Locate and identify every blood parasite.
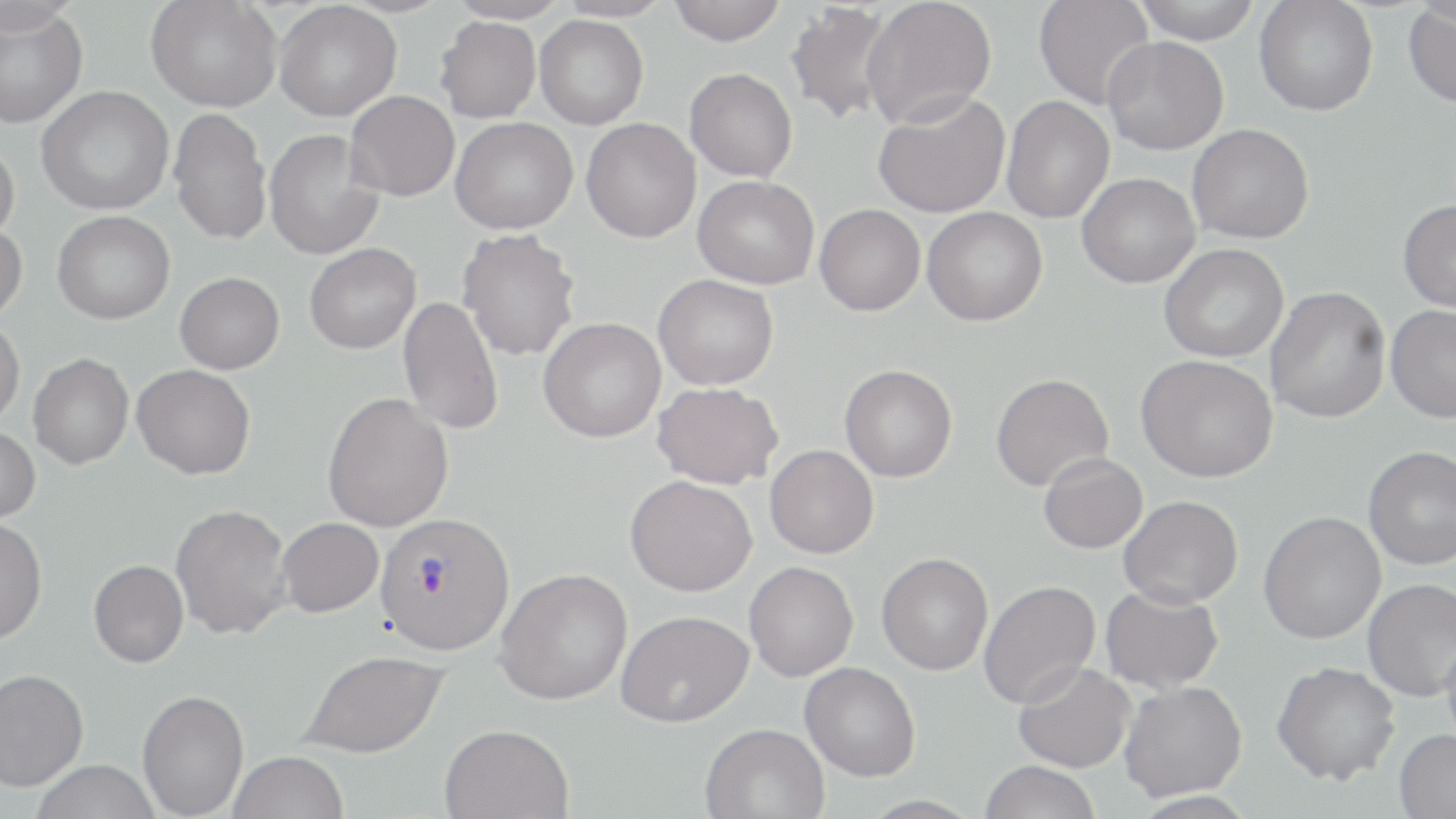
Approximate bounding boxes as [x1, y1, x2, y2] in pixels.
Plasmodium vivax-infected red blood cells: [374, 513, 514, 655].
No Plasmodium falciparum, Plasmodium ovale, Plasmodium malariae, Babesia divergens, or Trypanosoma brucei observed.

slide-level diagnosis = Plasmodium vivax
modality = light microscopy
image size = 1456×819 pixels
field of view = single
stain = May-Grünwald-Giemsa
uninfected red blood cell locations = approximate bounding boxes as [x1, y1, x2, y2] in pixels: [0, 0, 82, 35], [146, 0, 281, 112], [444, 0, 571, 25], [554, 0, 673, 23], [668, 0, 786, 45], [861, 0, 997, 128], [1034, 0, 1155, 110], [1132, 0, 1262, 44], [1254, 0, 1378, 116], [274, 2, 401, 121], [784, 2, 896, 126], [1403, 5, 1456, 107], [0, 7, 87, 128], [534, 15, 648, 129], [435, 16, 543, 123], [1102, 36, 1229, 155], [684, 68, 798, 182], [36, 86, 173, 215], [345, 91, 460, 201], [872, 92, 1011, 218], [1001, 96, 1114, 223], [168, 107, 271, 245], [450, 117, 577, 234], [581, 118, 701, 242], [1187, 124, 1314, 244], [264, 129, 384, 260], [0, 140, 19, 244], [1076, 173, 1200, 288], [692, 175, 819, 289], [1397, 199, 1456, 313], [814, 204, 925, 315], [922, 207, 1047, 326], [52, 211, 175, 324], [0, 223, 27, 325], [457, 228, 581, 361], [304, 243, 420, 354], [1159, 243, 1288, 362], [175, 272, 284, 374], [653, 274, 778, 390], [1264, 286, 1391, 423], [398, 295, 503, 435], [1385, 304, 1456, 422], [538, 317, 666, 442], [0, 319, 25, 429], [28, 353, 133, 469], [1136, 355, 1278, 482], [131, 364, 255, 479], [839, 364, 957, 482], [990, 373, 1113, 491], [652, 382, 783, 489], [322, 391, 453, 532], [0, 425, 40, 523], [765, 444, 878, 558], [1363, 446, 1456, 570], [1038, 452, 1147, 553], [625, 475, 757, 596], [1118, 495, 1243, 608], [170, 503, 293, 639], [1258, 510, 1386, 644], [0, 515, 47, 645], [277, 517, 384, 617], [876, 553, 993, 675], [89, 559, 188, 667], [744, 561, 858, 681], [495, 568, 633, 704], [1362, 578, 1456, 702], [978, 580, 1101, 708], [1100, 584, 1224, 693], [616, 610, 753, 727], [1441, 629, 1456, 753], [298, 650, 450, 758], [1012, 661, 1135, 772], [1271, 661, 1400, 785], [799, 662, 920, 781], [0, 668, 88, 791], [1118, 681, 1247, 802], [137, 689, 249, 818], [700, 722, 829, 819], [439, 723, 573, 818], [1394, 728, 1456, 819], [228, 751, 349, 819], [31, 759, 162, 819], [979, 760, 1101, 819], [1127, 790, 1260, 817]
preparation = thin blood smear
magnification = 1000x